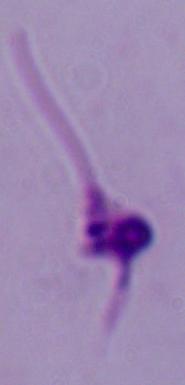
Summary:
  - Magnification: 1000x
  - Modality: photomicrograph
  - Identification: Leishmania